State which parasite is depicted.
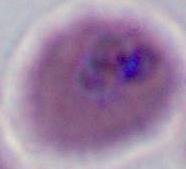
This is Plasmodium.

Summary:
  - Modality: photomicrograph
  - Magnification: 400x or 1000x